Describe the morphology of the red blood cells.
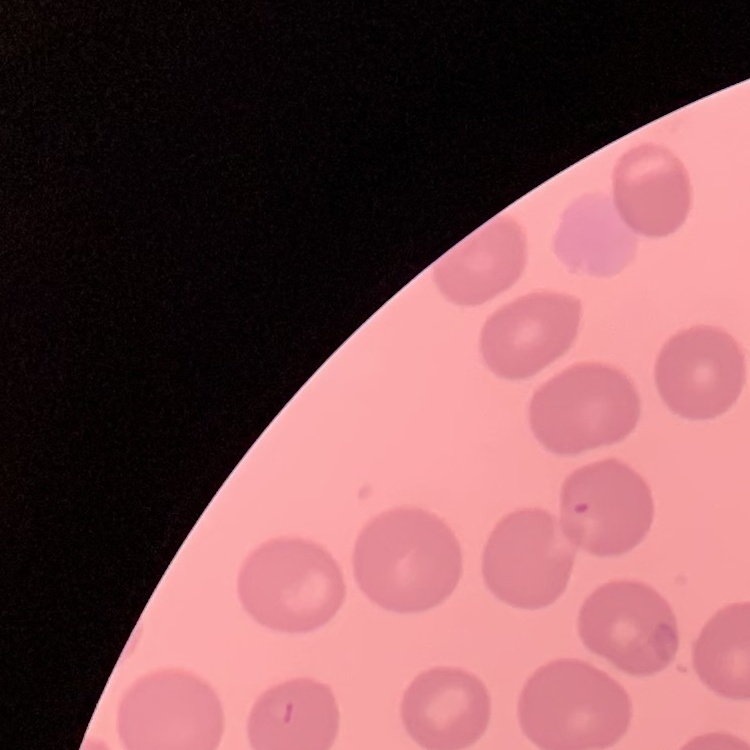

They show no rouleaux formation.

Thin blood film. Stained with either Field's or Giemsa. Square crop of a larger photomicrograph.